Identify the blood parasite species.
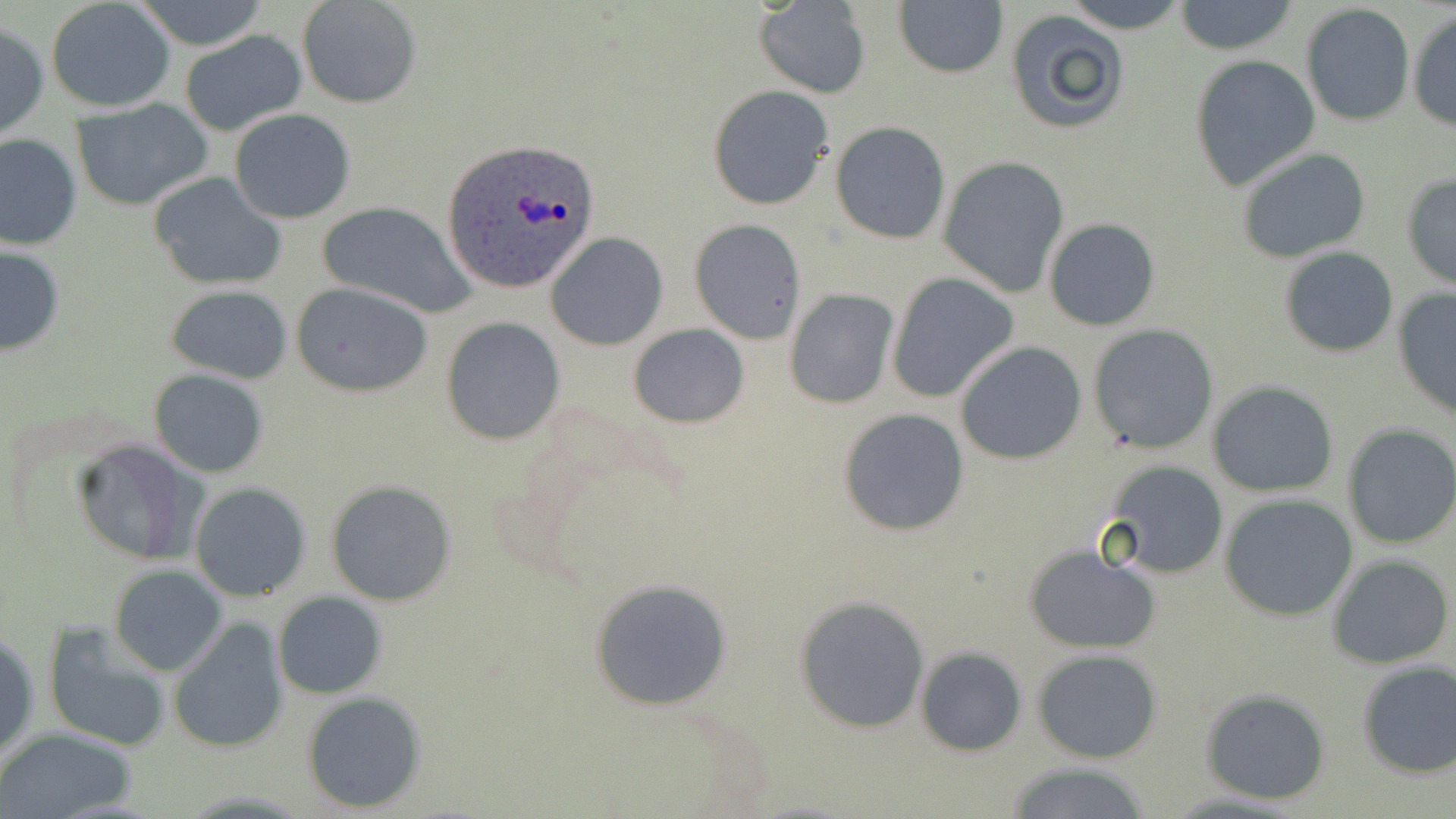
Plasmodium ovale.

modality = light microscopy
stain = May-Grünwald-Giemsa
Plasmodium ovale-infected red blood cell locations = approximate bounding boxes as [x1, y1, x2, y2] in pixels: [441, 138, 600, 295]
preparation = thin blood smear
magnification = 1000x
image size = 1456×819 pixels
uninfected red blood cell locations = approximate bounding boxes as [x1, y1, x2, y2] in pixels: [45, 0, 176, 113], [132, 0, 272, 51], [298, 0, 422, 108], [1058, 0, 1191, 32], [1173, 1, 1298, 55], [754, 2, 871, 97], [894, 2, 1008, 79], [1299, 4, 1416, 128], [1406, 9, 1456, 131], [1006, 11, 1130, 134], [0, 21, 49, 141], [180, 31, 308, 136], [1189, 54, 1320, 190], [707, 85, 834, 210], [69, 100, 214, 209], [228, 109, 356, 225], [831, 121, 950, 245], [0, 132, 81, 250], [1235, 147, 1371, 263], [939, 157, 1069, 298], [150, 171, 286, 290], [1400, 172, 1456, 290], [315, 201, 474, 317], [1043, 216, 1162, 331], [689, 218, 805, 345], [545, 233, 668, 351], [0, 244, 66, 356], [1278, 245, 1399, 358], [885, 272, 1019, 403], [289, 282, 433, 396], [165, 284, 293, 383], [783, 288, 898, 409], [1391, 288, 1455, 422], [441, 318, 566, 444], [628, 323, 750, 428], [1087, 324, 1218, 454], [955, 342, 1088, 465], [149, 368, 269, 478], [1206, 381, 1340, 498], [837, 407, 969, 536], [1342, 422, 1456, 550], [72, 438, 202, 565], [1102, 460, 1230, 579], [324, 479, 456, 606], [189, 482, 312, 602], [1219, 492, 1358, 621], [1023, 541, 1161, 654], [1327, 554, 1454, 669], [109, 564, 228, 676], [589, 576, 735, 710], [273, 591, 386, 699], [795, 597, 929, 733], [42, 620, 174, 754], [169, 620, 288, 753], [1, 627, 39, 765], [915, 647, 1027, 757], [1032, 648, 1165, 764], [1355, 660, 1455, 778], [1198, 688, 1333, 805], [300, 690, 427, 813], [0, 727, 140, 819], [1003, 761, 1161, 818]
field of view = single